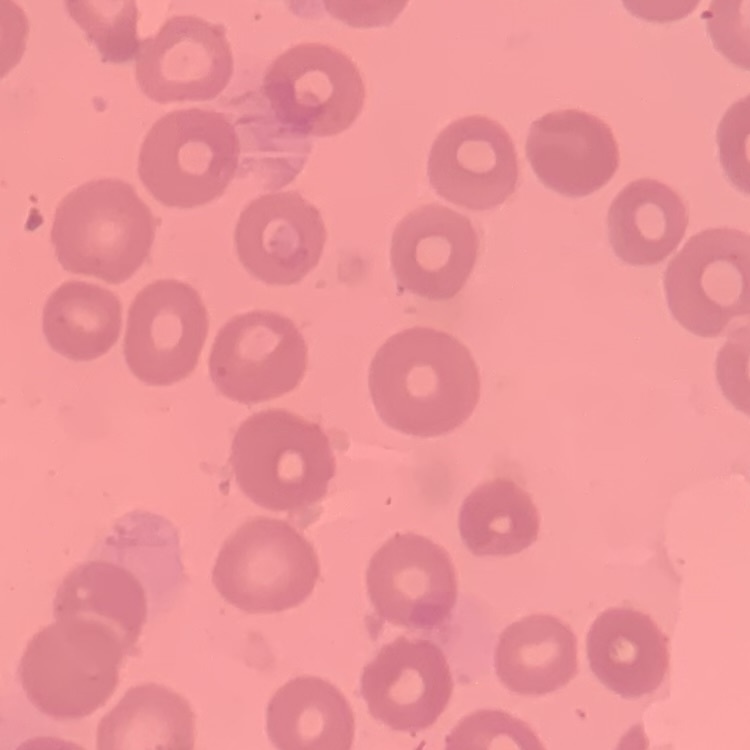 The erythrocytes show no rouleaux formation. Stained with either Field's or Giemsa. Thin blood smear. One tile cut from a larger photomicrograph.